Report the malaria status of this cell.
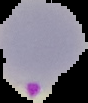
It is parasitized.

Image is 88×103 pixels. From a thin blood smear. The area outside the segmented cell region is set to black.